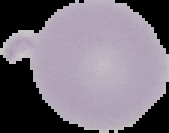

Summary:
  - Image size: 169×133 pixels
  - Image type: cell region segmented out of the field of view; surrounding area masked to black
  - Malaria status: uninfected
  - Preparation: thin blood film